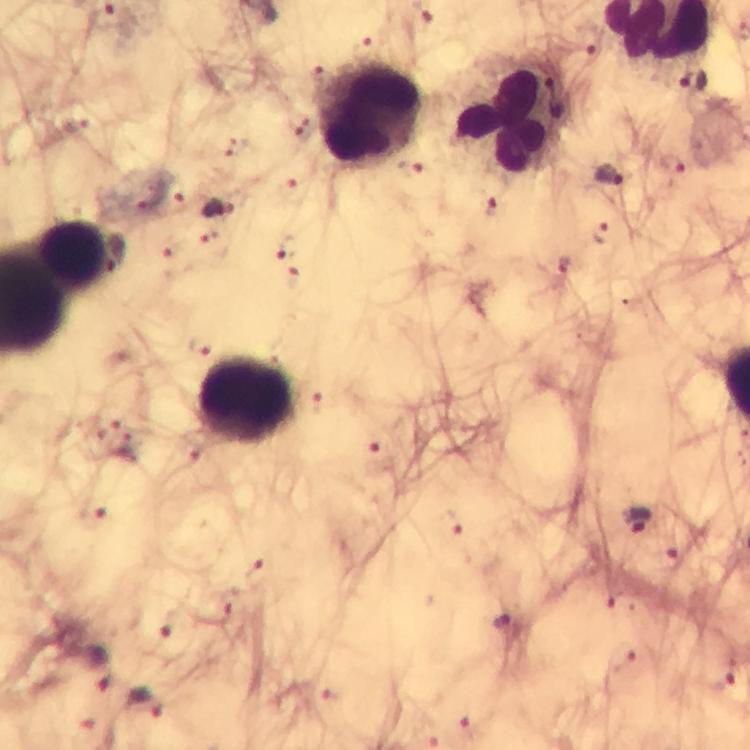
cropped_from: a single field of view
context: from a malaria diagnostic workup
stain: Giemsa
leukocyte_locations: 'approximate centers as (x, y) in pixels: (369, 114), (502, 119), (76, 254), (247, 399)'
preparation: thick smear
capture: smartphone mounted on the microscope
plasmodium_parasite_locations: 'approximate centers as (x, y) in pixels: (364, 46), (691, 82), (77, 122), (296, 124), (673, 165), (609, 176), (296, 194), (151, 199), (491, 208), (218, 210), (600, 233), (286, 248), (170, 254), (322, 402), (104, 426), (127, 446), (380, 452), (93, 515), (637, 520), (449, 521), (672, 557), (259, 571), (621, 603), (231, 606), (502, 623), (174, 625), (622, 658), (98, 667), (720, 681), (334, 697), (146, 703), (468, 726)'
immersion_oil: used
image_size: 750×750 pixels
magnification: 100x